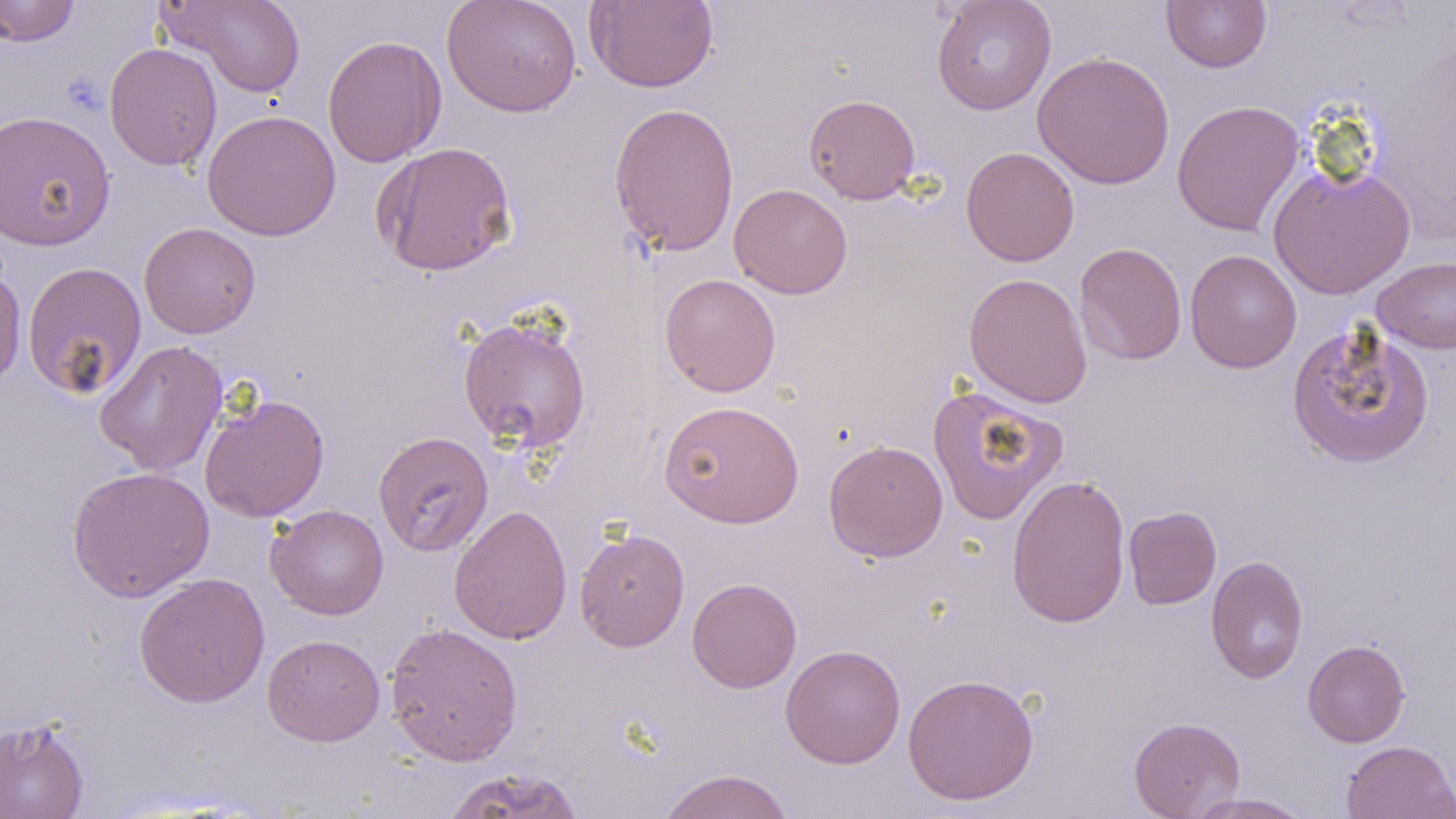
Summary:
  - Coordinate format: approximate bounding boxes as (x1, y1, x2, y2) in pixels
  - Uninfected red blood cell locations: (0, 0, 80, 47), (159, 0, 306, 98), (442, 0, 582, 117), (585, 0, 719, 93), (931, 0, 1057, 115), (1161, 1, 1272, 72), (321, 34, 447, 168), (103, 42, 222, 171), (1032, 50, 1175, 190), (804, 94, 921, 204), (1172, 99, 1305, 237), (608, 101, 740, 257), (202, 109, 341, 241), (0, 110, 116, 250), (372, 141, 518, 277), (960, 146, 1080, 267), (1267, 163, 1416, 300), (729, 183, 852, 299), (139, 223, 261, 339), (1074, 242, 1187, 366), (1185, 249, 1302, 373), (1372, 256, 1456, 354), (22, 260, 147, 400), (0, 263, 27, 393), (964, 272, 1092, 408), (659, 274, 781, 397), (458, 315, 593, 453), (1286, 321, 1435, 469), (94, 339, 228, 476), (927, 384, 1067, 525), (199, 393, 330, 522), (659, 399, 804, 528), (373, 431, 493, 556), (823, 439, 949, 562), (67, 465, 215, 602), (1006, 473, 1131, 628), (266, 504, 389, 620), (448, 504, 573, 645), (1123, 506, 1222, 609), (574, 528, 690, 652), (1206, 554, 1309, 684), (134, 571, 270, 708), (687, 577, 802, 693), (384, 622, 523, 766), (262, 634, 385, 746), (1302, 639, 1410, 747), (781, 644, 906, 769), (902, 673, 1039, 806), (0, 715, 90, 819), (1128, 716, 1246, 818), (1341, 740, 1456, 819), (440, 767, 586, 818), (658, 768, 794, 819), (1186, 793, 1314, 818)
  - Slide-level diagnosis: negative for blood parasites
  - Preparation: thin blood film
  - Stain: May-Grünwald-Giemsa
  - Field of view: one of a larger specimen
  - Modality: optical microscopy
  - Image size: 1456×819 pixels
  - Magnification: 1000x